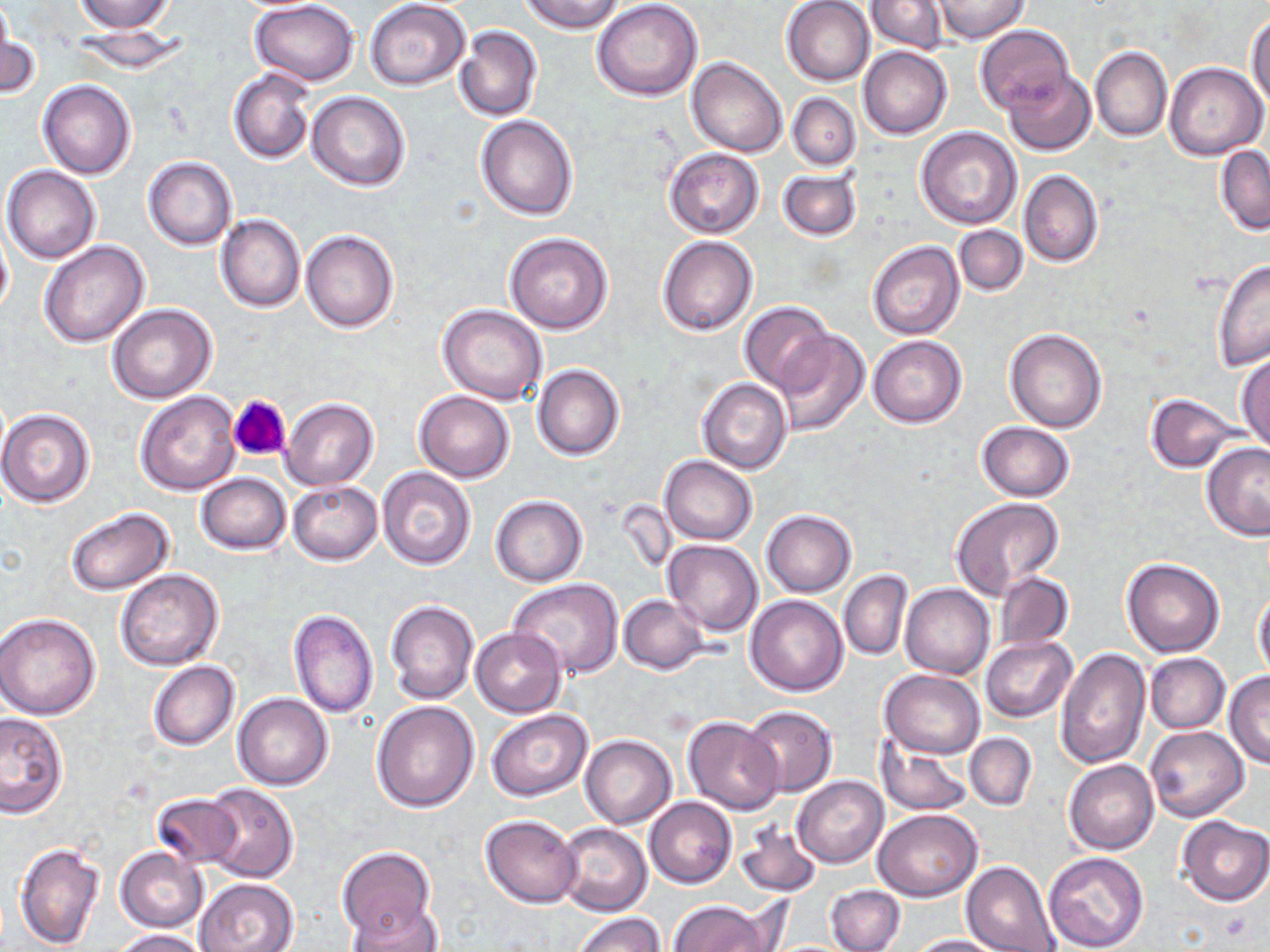

slide-level diagnosis = no evidence of blood parasites
magnification = 1000x
preparation = thin blood film
field of view = single
uninfected red blood cell locations = approximate bounding boxes as named x1/y1/x2/y2 corners in pixels: (x1=0, y1=0, x2=15, y2=76), (x1=74, y1=0, x2=176, y2=33), (x1=249, y1=0, x2=359, y2=85), (x1=522, y1=0, x2=624, y2=34), (x1=867, y1=0, x2=949, y2=53), (x1=365, y1=1, x2=470, y2=89), (x1=592, y1=1, x2=704, y2=102), (x1=782, y1=1, x2=875, y2=86), (x1=933, y1=1, x2=1029, y2=44), (x1=1247, y1=13, x2=1270, y2=110), (x1=71, y1=25, x2=191, y2=75), (x1=976, y1=25, x2=1073, y2=114), (x1=455, y1=26, x2=543, y2=123), (x1=1, y1=28, x2=40, y2=100), (x1=858, y1=47, x2=951, y2=139), (x1=1090, y1=47, x2=1171, y2=142), (x1=687, y1=56, x2=787, y2=157), (x1=1163, y1=62, x2=1266, y2=159), (x1=228, y1=69, x2=316, y2=164), (x1=1004, y1=70, x2=1095, y2=156), (x1=39, y1=80, x2=136, y2=181), (x1=305, y1=90, x2=410, y2=190), (x1=787, y1=93, x2=860, y2=170), (x1=475, y1=114, x2=579, y2=220), (x1=916, y1=127, x2=1023, y2=230), (x1=1214, y1=145, x2=1269, y2=235), (x1=664, y1=147, x2=764, y2=238), (x1=143, y1=156, x2=237, y2=249), (x1=3, y1=166, x2=101, y2=264), (x1=777, y1=166, x2=862, y2=243), (x1=1019, y1=171, x2=1102, y2=267), (x1=215, y1=213, x2=305, y2=313), (x1=0, y1=225, x2=13, y2=316), (x1=954, y1=225, x2=1026, y2=295), (x1=301, y1=230, x2=400, y2=333), (x1=505, y1=232, x2=613, y2=334), (x1=658, y1=236, x2=758, y2=337), (x1=38, y1=240, x2=149, y2=347), (x1=867, y1=241, x2=964, y2=340), (x1=1213, y1=257, x2=1270, y2=371), (x1=108, y1=303, x2=218, y2=404), (x1=438, y1=304, x2=548, y2=405), (x1=740, y1=304, x2=833, y2=391), (x1=1004, y1=328, x2=1108, y2=432), (x1=773, y1=331, x2=869, y2=437), (x1=867, y1=335, x2=967, y2=429), (x1=1236, y1=353, x2=1269, y2=453), (x1=532, y1=364, x2=624, y2=461), (x1=697, y1=377, x2=790, y2=473), (x1=134, y1=390, x2=241, y2=496), (x1=414, y1=391, x2=515, y2=483), (x1=1146, y1=393, x2=1244, y2=473), (x1=281, y1=398, x2=378, y2=489), (x1=0, y1=409, x2=95, y2=507), (x1=976, y1=422, x2=1074, y2=501), (x1=1201, y1=442, x2=1270, y2=540), (x1=660, y1=456, x2=757, y2=544), (x1=376, y1=467, x2=476, y2=570), (x1=196, y1=472, x2=291, y2=554), (x1=287, y1=481, x2=382, y2=565), (x1=491, y1=496, x2=587, y2=587), (x1=950, y1=497, x2=1063, y2=596), (x1=65, y1=507, x2=174, y2=595), (x1=761, y1=510, x2=856, y2=597), (x1=663, y1=539, x2=763, y2=635), (x1=1121, y1=556, x2=1225, y2=657), (x1=115, y1=568, x2=223, y2=670), (x1=839, y1=569, x2=913, y2=661), (x1=996, y1=572, x2=1072, y2=650), (x1=506, y1=580, x2=623, y2=678), (x1=899, y1=582, x2=994, y2=679), (x1=1253, y1=589, x2=1270, y2=680), (x1=619, y1=595, x2=708, y2=674), (x1=746, y1=595, x2=848, y2=696), (x1=385, y1=599, x2=480, y2=705), (x1=288, y1=609, x2=378, y2=718), (x1=0, y1=613, x2=101, y2=720), (x1=470, y1=627, x2=566, y2=717), (x1=981, y1=637, x2=1076, y2=722), (x1=1057, y1=647, x2=1150, y2=769), (x1=1145, y1=653, x2=1229, y2=733), (x1=148, y1=660, x2=239, y2=751), (x1=879, y1=669, x2=984, y2=758), (x1=1224, y1=671, x2=1270, y2=768), (x1=233, y1=694, x2=332, y2=790), (x1=371, y1=700, x2=479, y2=812), (x1=742, y1=705, x2=836, y2=797), (x1=486, y1=710, x2=591, y2=802), (x1=0, y1=712, x2=68, y2=818), (x1=683, y1=715, x2=785, y2=815), (x1=1145, y1=724, x2=1249, y2=822), (x1=965, y1=733, x2=1036, y2=810), (x1=581, y1=735, x2=677, y2=828), (x1=876, y1=738, x2=974, y2=816), (x1=1064, y1=759, x2=1158, y2=854), (x1=792, y1=776, x2=888, y2=867), (x1=201, y1=784, x2=298, y2=882), (x1=151, y1=792, x2=241, y2=870), (x1=645, y1=797, x2=737, y2=889), (x1=873, y1=808, x2=983, y2=900), (x1=480, y1=813, x2=582, y2=908), (x1=1178, y1=816, x2=1270, y2=905), (x1=555, y1=821, x2=652, y2=916), (x1=736, y1=822, x2=821, y2=896), (x1=13, y1=840, x2=105, y2=952), (x1=337, y1=846, x2=435, y2=944), (x1=114, y1=847, x2=208, y2=932), (x1=1043, y1=851, x2=1149, y2=952), (x1=961, y1=861, x2=1060, y2=952), (x1=195, y1=878, x2=300, y2=952), (x1=826, y1=884, x2=904, y2=951), (x1=346, y1=899, x2=440, y2=950), (x1=669, y1=900, x2=774, y2=952), (x1=571, y1=911, x2=665, y2=952), (x1=113, y1=929, x2=212, y2=952), (x1=906, y1=934, x2=1007, y2=952)
stain = May-Grünwald-Giemsa
image size = 1270×952 pixels
modality = optical microscopy
platelet locations = approximate bounding boxes as named x1/y1/x2/y2 corners in pixels: (x1=228, y1=394, x2=293, y2=463)